Identify the blood parasite species.
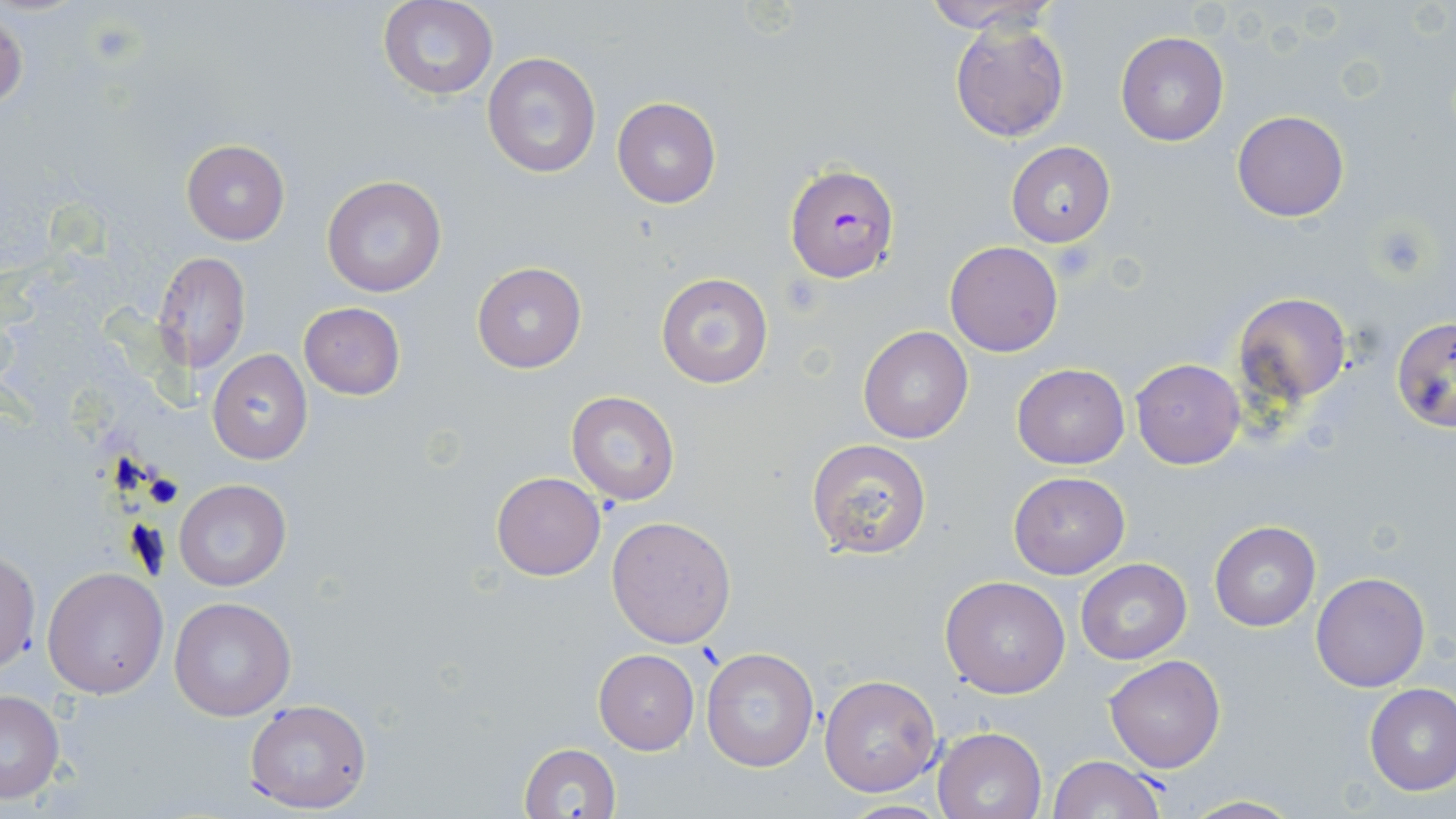

Plasmodium falciparum.

image size = 1456×819 pixels
preparation = thin blood smear
modality = optical microscopy
magnification = 1000x
stain = May-Grünwald-Giemsa
platelet locations = approximate bounding boxes as (x1, y1, x2, y2) in pixels: (1369, 223, 1430, 279), (1051, 241, 1098, 282)
uninfected red blood cell locations = approximate bounding boxes as (x1, y1, x2, y2) in pixels: (921, 0, 1059, 32), (378, 1, 498, 100), (1, 12, 26, 113), (950, 17, 1070, 142), (1115, 30, 1230, 147), (481, 51, 602, 180), (612, 97, 721, 208), (1232, 110, 1349, 222), (181, 140, 289, 243), (1005, 142, 1115, 247), (322, 174, 449, 298), (944, 241, 1064, 357), (155, 251, 251, 373), (472, 261, 587, 374), (655, 272, 774, 390), (1231, 291, 1351, 406), (298, 301, 404, 401), (1392, 317, 1456, 434), (858, 325, 973, 444), (207, 349, 312, 464), (1131, 358, 1245, 469), (1011, 362, 1130, 469), (566, 392, 680, 506), (806, 437, 932, 559), (1007, 469, 1130, 579), (492, 472, 604, 581), (173, 477, 292, 592), (606, 515, 736, 649), (1210, 521, 1321, 631), (0, 551, 40, 673), (1076, 559, 1192, 664), (42, 566, 167, 699), (1311, 571, 1430, 693), (940, 576, 1071, 698), (168, 598, 295, 721), (700, 646, 818, 773), (593, 648, 700, 755), (1103, 656, 1225, 773), (820, 675, 942, 795), (1364, 684, 1456, 796), (0, 689, 65, 804), (244, 699, 373, 813), (933, 725, 1047, 819), (518, 742, 621, 819), (1048, 755, 1164, 819), (1176, 794, 1306, 818), (837, 801, 955, 818)
field of view = single
Plasmodium falciparum-infected red blood cell locations = approximate bounding boxes as (x1, y1, x2, y2) in pixels: (784, 164, 900, 284)